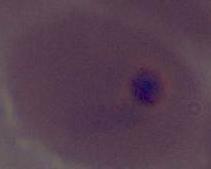

Captured at either 400x or 1000x magnification. Micrograph. A Plasmodium parasite is shown.